Classify this cell by malaria status.
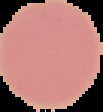
Uninfected.

image size = 103×112 pixels
image type = segmented cell region with the area outside set to black
preparation = thin blood film